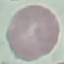

malaria status = uninfected
image type = cell patch, automatically extracted from a larger field of view and resized to 64 × 64 pixels
preparation = thin smear
stain = Giemsa
capture = smartphone camera at the microscope eyepiece